Mark where platelets are.
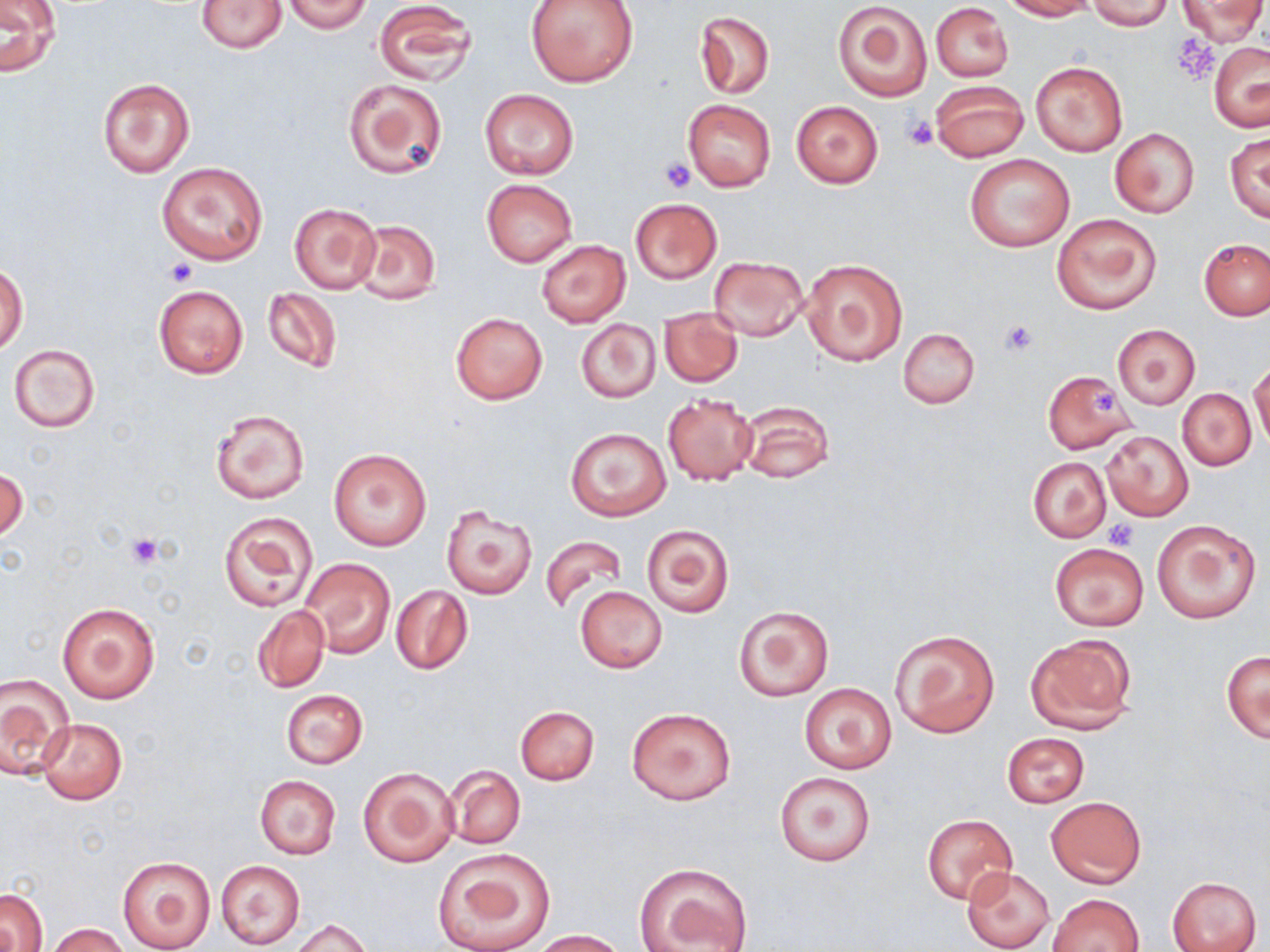

Approximate bounding boxes as (x1, y1, x2, y2) in pixels.
Platelets: (1173, 34, 1218, 81), (901, 115, 937, 151), (661, 157, 695, 193), (165, 259, 196, 287), (999, 318, 1040, 356), (1092, 390, 1115, 415), (1106, 519, 1138, 549), (125, 533, 165, 569).

slide_level_diagnosis: negative for blood parasites
field_of_view: single
uninfected_red_blood_cell_locations: 'approximate bounding boxes as (x1, y1, x2, y2) in pixels: (196, 0, 288, 53), (283, 0, 373, 33), (526, 0, 638, 88), (1003, 0, 1095, 20), (1087, 0, 1173, 30), (1179, 0, 1265, 45), (373, 1, 476, 87), (830, 2, 931, 101), (0, 3, 61, 75), (930, 3, 1013, 81), (695, 11, 774, 99), (1209, 41, 1270, 130), (1031, 62, 1127, 156), (342, 76, 447, 178), (98, 77, 195, 176), (930, 80, 1028, 161), (479, 87, 579, 180), (683, 100, 775, 191), (792, 100, 883, 188), (1110, 128, 1200, 218), (1225, 133, 1270, 224), (964, 153, 1075, 252), (156, 161, 268, 265), (481, 179, 577, 266), (629, 197, 722, 284), (290, 202, 382, 295), (1052, 214, 1161, 314), (349, 220, 441, 306), (1199, 238, 1269, 321), (537, 240, 630, 326), (709, 255, 807, 341), (800, 258, 908, 367), (1, 263, 28, 354), (153, 285, 248, 379), (261, 287, 342, 373), (659, 308, 742, 388), (449, 310, 549, 406), (576, 319, 661, 403), (1113, 324, 1200, 409), (898, 327, 979, 409), (8, 343, 100, 432), (1250, 361, 1269, 452), (1041, 370, 1137, 454), (1178, 388, 1256, 471), (662, 394, 757, 485), (739, 400, 834, 485), (210, 408, 310, 504), (564, 428, 671, 520), (1104, 432, 1193, 520), (327, 447, 433, 552), (1028, 456, 1111, 542), (1, 467, 28, 543), (441, 505, 538, 599), (219, 512, 315, 612), (1152, 519, 1263, 624), (641, 524, 735, 617), (540, 535, 628, 613), (1049, 543, 1149, 631), (301, 557, 394, 660), (391, 585, 473, 675), (575, 587, 667, 673), (58, 602, 160, 703), (252, 604, 330, 693), (732, 606, 833, 701), (889, 629, 1000, 738), (1025, 634, 1137, 733), (1221, 650, 1269, 742), (0, 675, 73, 781), (798, 682, 899, 775), (280, 688, 367, 769), (515, 705, 600, 785), (627, 707, 736, 806), (38, 717, 128, 804), (1003, 732, 1090, 808), (445, 765, 526, 850), (357, 766, 458, 867), (774, 770, 876, 868), (254, 775, 341, 859), (1047, 796, 1145, 888), (922, 813, 1018, 904), (432, 848, 556, 952), (117, 854, 217, 951), (214, 859, 305, 950), (633, 862, 752, 952), (961, 866, 1055, 950), (1168, 876, 1262, 952), (1, 888, 48, 952), (1048, 893, 1143, 952), (289, 918, 372, 952), (47, 923, 129, 952), (530, 930, 628, 951)'
modality: light microscopy
preparation: thin blood smear
stain: May-Grünwald-Giemsa
magnification: 1000x
image_size: 1270×952 pixels